Point out each Plasmodium parasite.
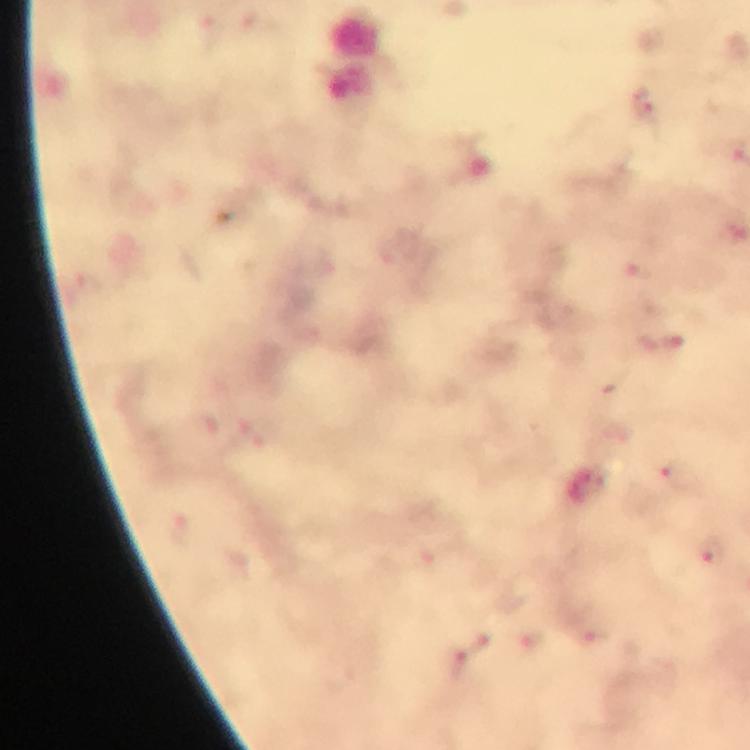
Approximate object centers, in pixels from the top-left corner.
Plasmodium parasites: (x=640, y=104), (x=639, y=271), (x=672, y=343), (x=678, y=473), (x=714, y=554), (x=456, y=662).

preparation = thick blood film
immersion oil = used
magnification = 100x
capture = smartphone photograph through a microscope
stain = Giemsa
image size = 750×750 pixels
context = from a malaria diagnostic workup
cropped from = one field of view